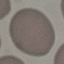
result = no malaria parasites seen
image type = automatically extracted cell patch, resized to 64 × 64 pixels
stain = Giemsa
capture = smartphone camera at the microscope eyepiece
preparation = thin smear